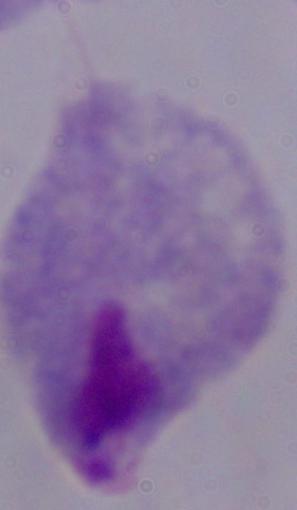
modality = photomicrograph
magnification = 1000x
identification = trichomonad